Locate every leukocyte (white blood cell).
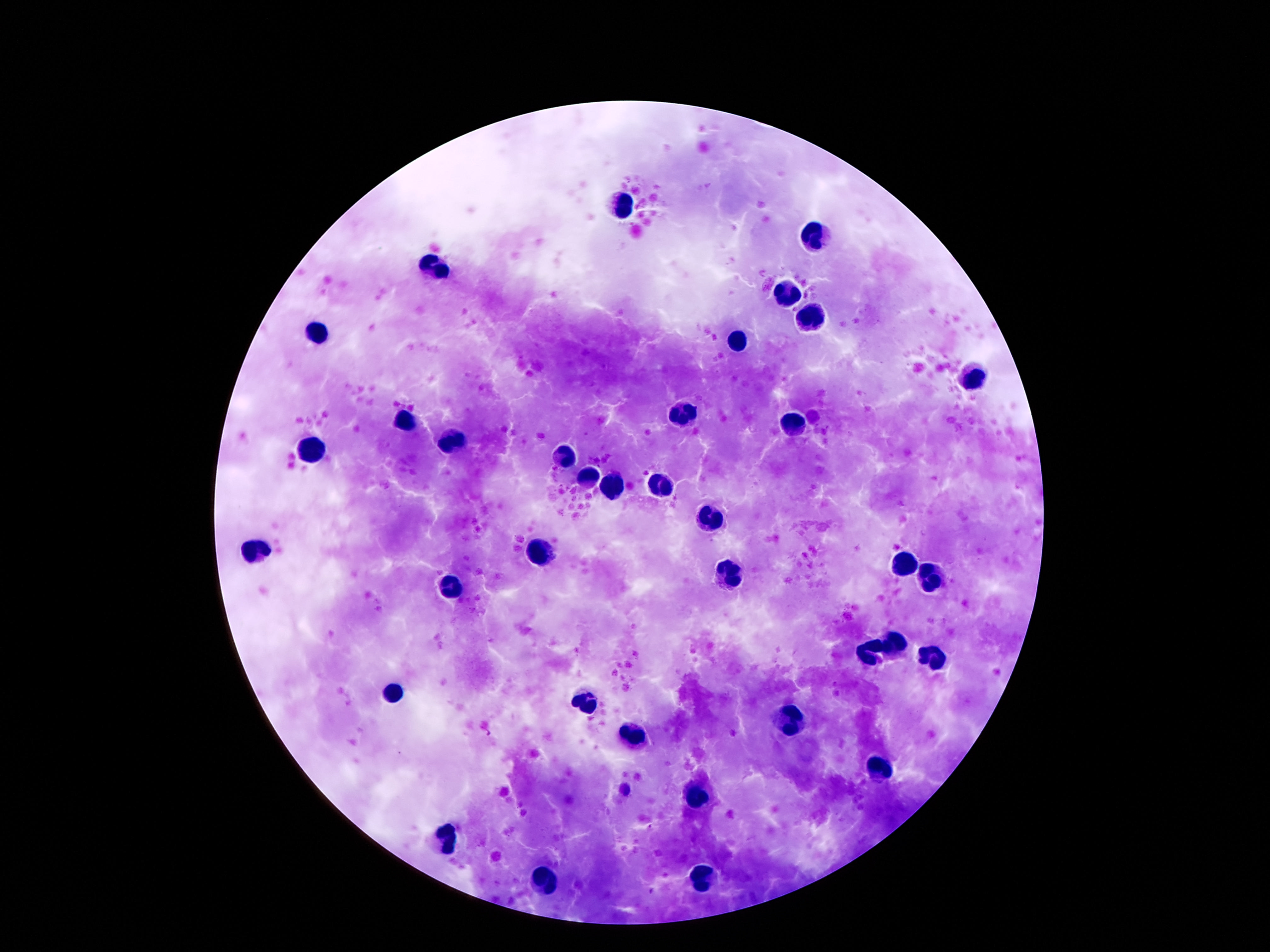
Approximate object centers, in pixels from the top-left corner.
Leukocytes: (x=622, y=203), (x=809, y=237), (x=435, y=267), (x=786, y=294), (x=811, y=321), (x=315, y=331), (x=737, y=340), (x=969, y=376), (x=681, y=415), (x=399, y=419), (x=794, y=423), (x=448, y=445), (x=309, y=449), (x=563, y=460), (x=584, y=477), (x=660, y=485), (x=609, y=489), (x=710, y=515), (x=261, y=550), (x=542, y=550), (x=901, y=563), (x=733, y=575), (x=933, y=577), (x=456, y=588), (x=895, y=643), (x=866, y=652), (x=931, y=659), (x=393, y=694), (x=586, y=703), (x=792, y=721), (x=635, y=736), (x=882, y=769), (x=698, y=799), (x=443, y=837), (x=546, y=881), (x=706, y=881).

100x magnification. One field from this slide. Giemsa-stained preparation. Image is 1270×952 pixels. Patient malaria status: uninfected. Thick peripheral-blood smear. Photographed through the microscope eyepiece with a smartphone camera.